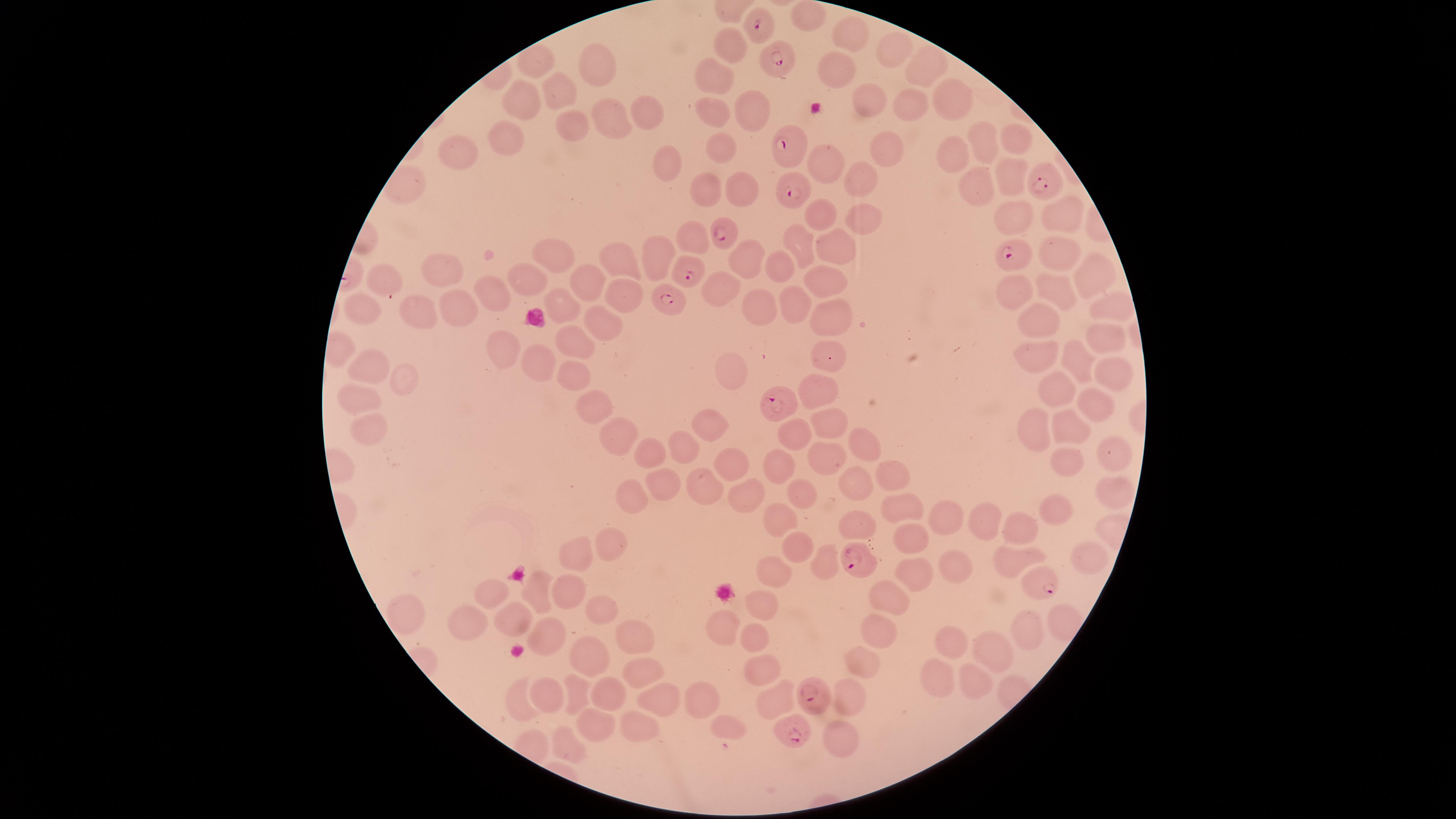

Approximate marker points as [x, y] in pixels. Uninfected red blood cells: [847, 32], [730, 40], [900, 47], [596, 65], [927, 67], [834, 74], [713, 78], [556, 93], [870, 93], [524, 96], [960, 101], [911, 104], [748, 108], [647, 110], [713, 110], [614, 115], [568, 128], [1022, 135], [990, 138], [507, 140], [723, 145], [460, 148], [882, 148], [664, 154], [958, 155], [823, 160], [856, 177], [1007, 181], [707, 189], [738, 189], [979, 190], [1008, 215], [1064, 215], [827, 216], [859, 218], [694, 238], [800, 248], [1056, 248], [836, 250], [553, 255], [751, 255], [653, 257], [616, 258], [777, 268], [437, 272], [383, 274], [821, 279], [1090, 279], [531, 282], [585, 284], [719, 287], [1062, 287], [1014, 288], [623, 292], [485, 297], [762, 304], [1110, 305], [419, 306], [566, 306], [795, 306], [457, 308], [365, 311], [827, 316], [600, 321], [1050, 322], [1103, 336], [571, 344], [500, 346], [1078, 352], [1034, 353], [826, 360], [541, 361], [364, 365], [577, 370], [734, 372], [400, 373], [1111, 378], [818, 390], [1049, 393], [353, 400], [1091, 401], [596, 408], [825, 419], [369, 424], [710, 427], [1031, 431], [1070, 432], [615, 433], [791, 437], [863, 447], [653, 450], [684, 450], [822, 454], [732, 457], [1108, 457], [782, 463], [1068, 465], [893, 476], [855, 482], [660, 486], [703, 489], [750, 494], [1104, 494], [631, 496], [800, 499], [898, 508], [1052, 511], [980, 520], [773, 522], [944, 522], [1020, 527], [859, 528], [903, 537], [612, 542], [577, 552], [794, 552], [1011, 555], [1088, 559], [820, 561], [953, 563], [772, 573], [906, 580], [541, 584], [566, 591], [494, 593], [885, 598], [758, 607], [598, 608], [466, 612], [512, 613], [722, 624], [1029, 624], [550, 632], [748, 638], [631, 639], [873, 639], [951, 643], [995, 653], [590, 654], [859, 663], [755, 669], [647, 674], [939, 683], [977, 684], [573, 689], [609, 689], [848, 692], [696, 696], [548, 697], [771, 699], [656, 703], [728, 722], [596, 724], [637, 733], [836, 738], [562, 742]. Parasitized red blood cells: [756, 27], [778, 60], [789, 143], [1042, 187], [792, 193], [720, 234], [1011, 257], [688, 273], [666, 299], [785, 400], [857, 564], [1040, 583], [809, 693], [790, 733]. Image is 1456×819 pixels. Smartphone photograph through the microscope eyepiece. Giemsa-stained preparation. Presence: malaria parasites identified. Single field of view. Thin blood film. Species: Plasmodium falciparum. The visible region is circular.